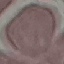

Summary:
  - Malaria status: uninfected
  - Preparation: thin blood film
  - Capture: smartphone through the microscope eyepiece
  - Stain: Giemsa
  - Image type: automatically extracted cell patch, resized to 64 × 64 pixels